Comment on the morphology of the erythrocytes.
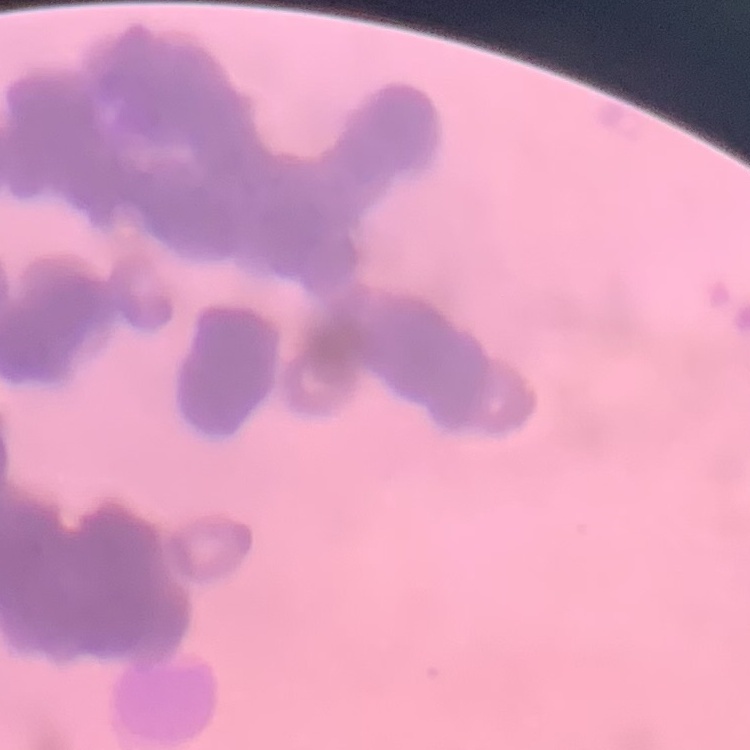
Rouleaux formation.

{
  "stain": "Field's or Giemsa",
  "image_type": "square crop of a larger photomicrograph",
  "preparation": "thin blood film"
}